Assess the morphology of the erythrocytes.
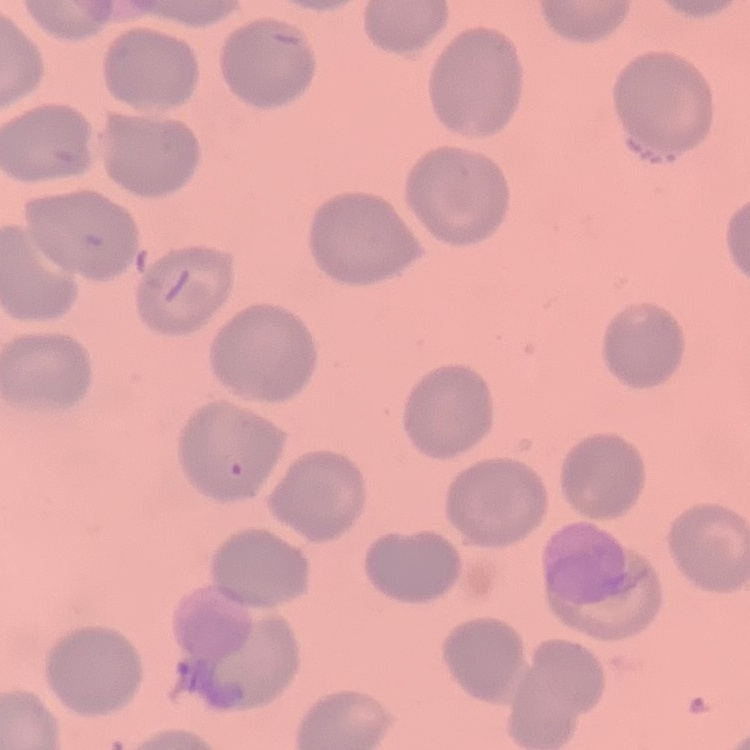
No rouleaux formation.

Thin blood film. Stained with either Field's or Giemsa. One tile cut from a larger photomicrograph.